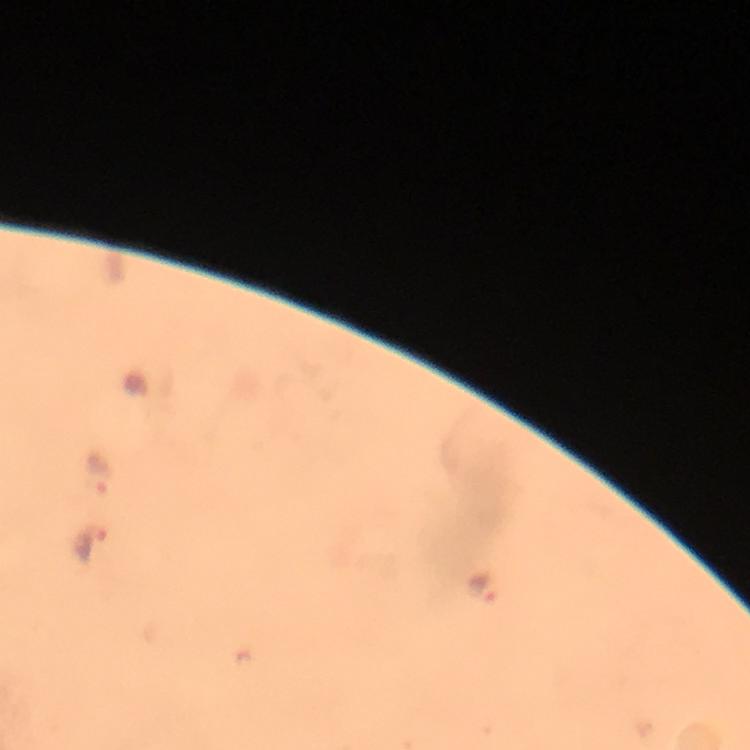

Approximate centers as {x, y} in pixels.
Summary:
  - Plasmodium parasite locations: {99, 472}, {90, 545}, {484, 589}
  - Magnification: 100x
  - Preparation: thick blood smear
  - Cropped from: a single field of view
  - Immersion oil: applied
  - Context: from a diagnostic examination for malaria
  - Image size: 750×750 pixels
  - Stain: Giemsa
  - Capture: smartphone mounted on the microscope